Locate every malaria parasite.
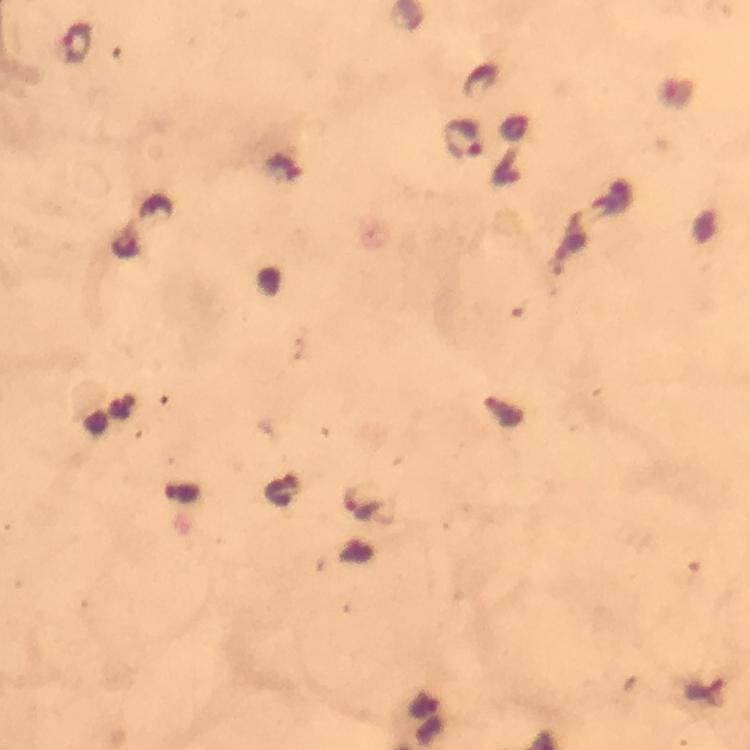
Approximate object centers, in pixels from the top-left corner.
Malaria parasites: (x=76, y=44), (x=464, y=140), (x=125, y=247), (x=359, y=504).

Thick blood smear. From a malaria diagnostic workup. Photographed with a smartphone mounted on the microscope. Immersion oil applied. Image is 750×750 pixels. A crop from one field of view. Giemsa stain. 100x magnification.